Give the extent of all Plasmodium vivax-infected red blood cells.
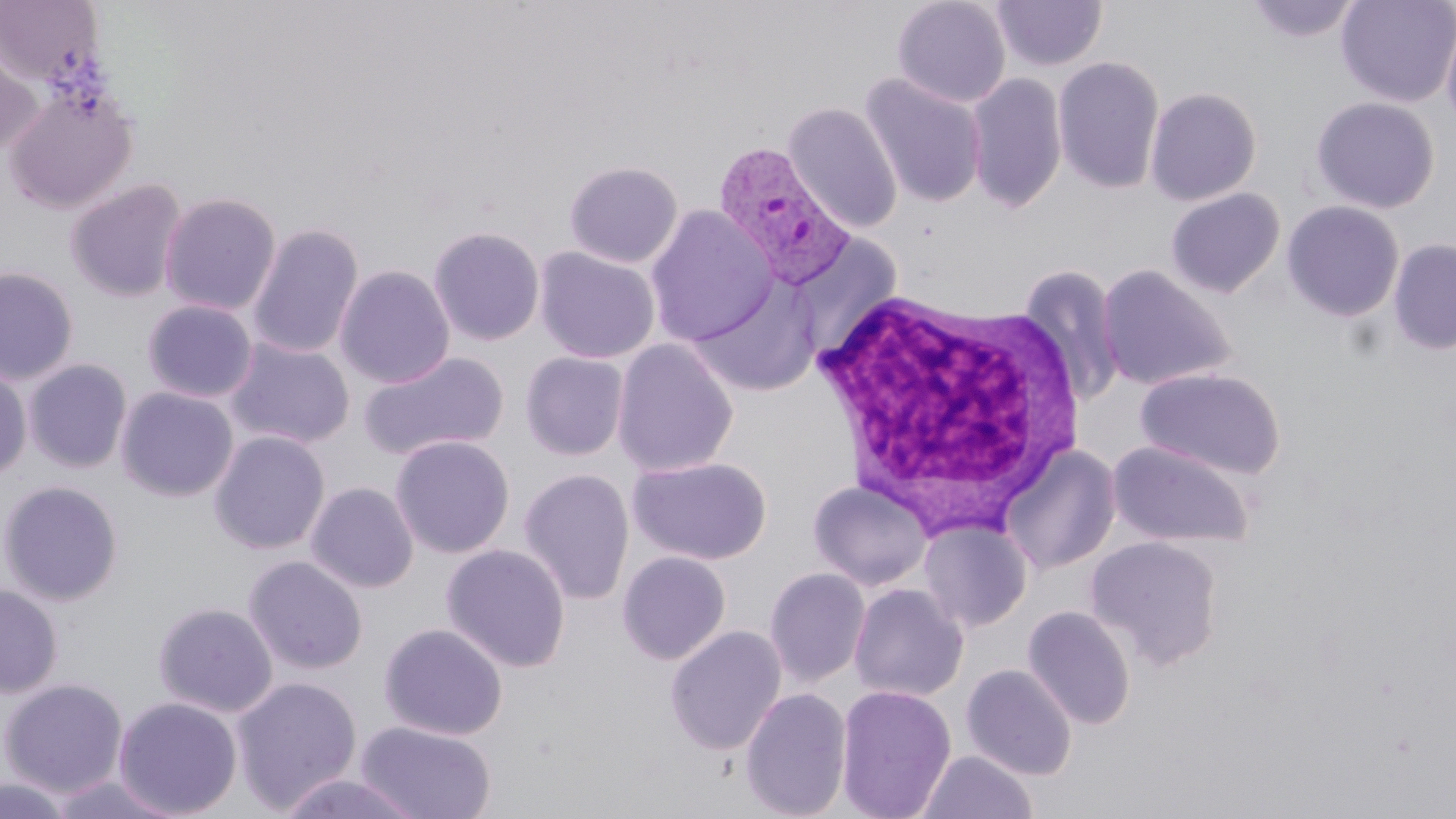
Approximate bounding boxes as (x1,y1)-(x2,y2) corner pairs in pixels.
Plasmodium vivax-infected red blood cells: (713,142)-(854,288).

Summary:
  - Uninfected red blood cell locations: (892,0)-(1012,108), (991,0)-(1108,70), (1245,0)-(1363,43), (1336,0)-(1456,107), (0,1)-(105,87), (1441,10)-(1456,137), (1,38)-(42,156), (1053,56)-(1165,194), (860,73)-(988,208), (965,73)-(1067,214), (4,87)-(138,213), (1145,87)-(1262,205), (1311,97)-(1440,213), (783,102)-(902,234), (564,161)-(683,268), (65,178)-(188,302), (1166,188)-(1284,297), (158,191)-(282,316), (1165,193)-(1407,307), (1282,201)-(1404,321), (644,205)-(778,347), (247,223)-(364,359), (428,226)-(545,346), (788,233)-(903,360), (1388,238)-(1456,356), (534,246)-(660,364), (1097,264)-(1236,391), (335,265)-(455,388), (1018,265)-(1125,409), (0,266)-(79,385), (689,276)-(822,397), (142,299)-(258,402), (225,338)-(355,448), (612,338)-(739,477), (358,350)-(509,461), (520,352)-(629,461), (23,358)-(133,474), (0,365)-(31,482), (1136,367)-(1286,480), (116,387)-(238,502), (209,430)-(330,555), (390,435)-(514,558), (1107,440)-(1254,548), (1000,444)-(1121,575), (627,456)-(773,565), (518,468)-(635,605), (0,480)-(123,605), (808,480)-(933,591), (305,482)-(419,593), (919,518)-(1033,633), (1086,536)-(1224,669), (441,543)-(571,673), (617,551)-(731,664), (243,555)-(368,675), (764,567)-(870,689), (848,583)-(969,702), (0,584)-(63,698), (153,602)-(278,717), (1022,606)-(1136,729), (379,623)-(508,740), (665,625)-(787,756), (961,664)-(1077,780), (231,676)-(362,814), (0,678)-(128,797), (835,684)-(957,819), (739,687)-(853,819), (112,696)-(243,817), (356,721)-(496,819), (917,750)-(1038,819), (273,772)-(425,819), (46,774)-(184,818), (0,775)-(74,818)
  - White blood cell locations: (801,286)-(1094,536)
  - Slide-level diagnosis: Plasmodium vivax
  - Stain: May-Grünwald-Giemsa
  - Magnification: 1000x
  - Preparation: thin blood film
  - Image size: 1456×819 pixels
  - Modality: light microscopy
  - Field of view: one of a larger specimen